Describe the morphology of the erythrocytes.
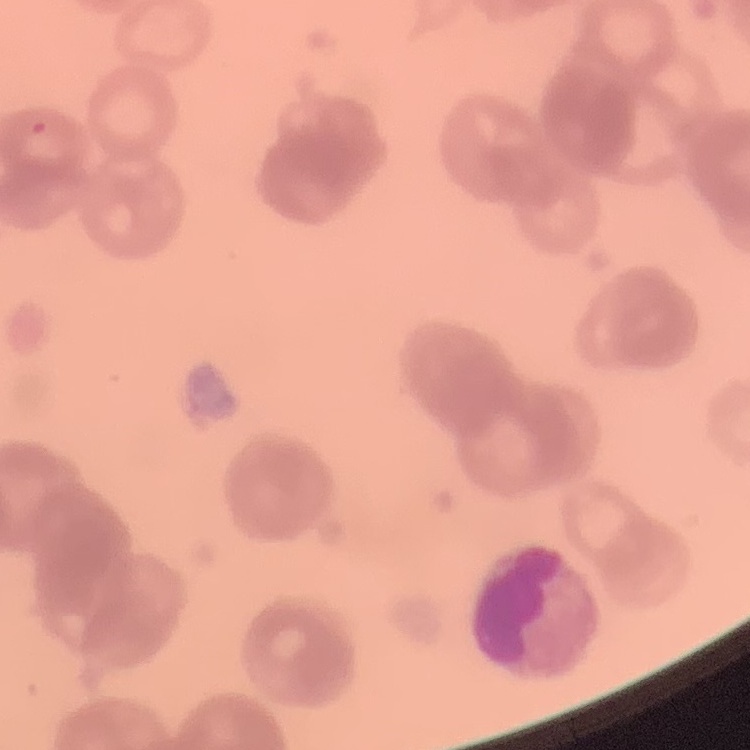

Rouleaux formation.

image type = one tile cut from a larger photomicrograph
preparation = thin blood smear
stain = Field's or Giemsa